Comment on the morphology of the erythrocytes.
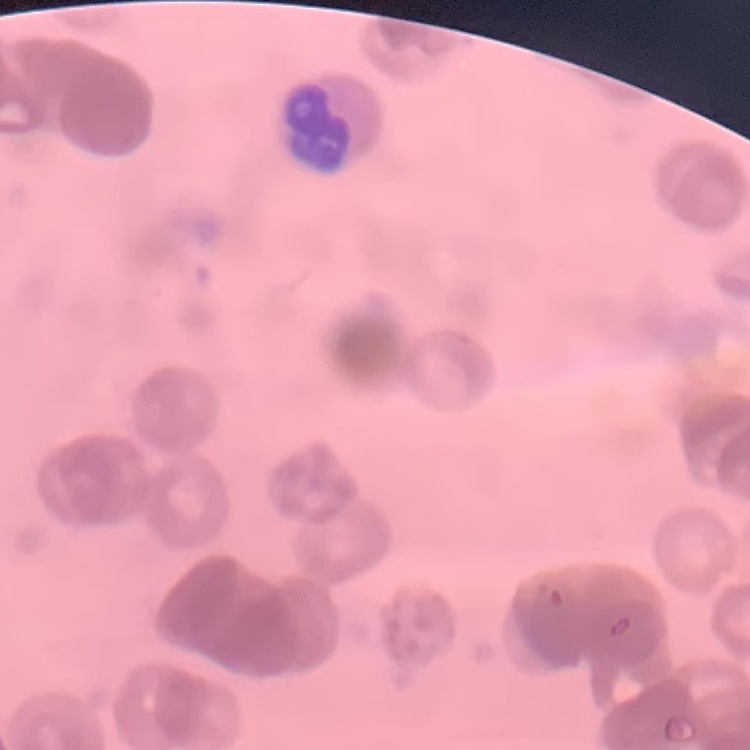

Rouleaux formation.

One tile cut from a larger photomicrograph. Thin blood film. Field's or Giemsa stain.